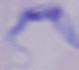 A trypanosome is shown. Captured at 1000x magnification. Micrograph.